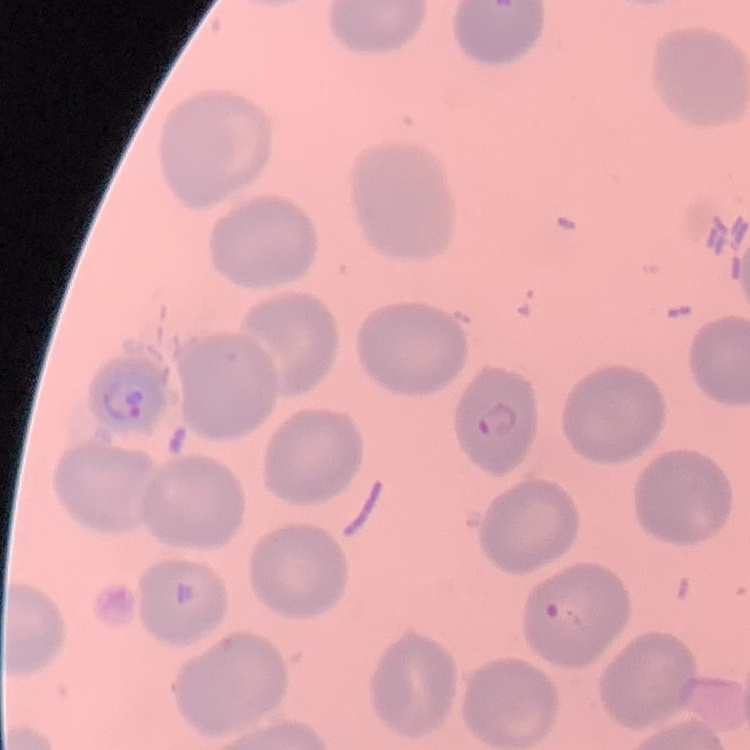

Summary:
  - Erythrocyte morphology: no rouleaux formation
  - Image type: square crop of a larger photomicrograph
  - Preparation: thin blood film
  - Stain: Field's or Giemsa